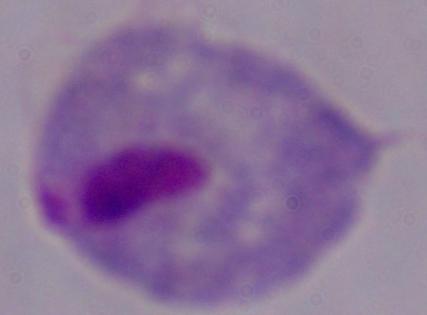

{
  "modality": "photomicrograph",
  "magnification": "1000x",
  "identification": "trichomonad"
}